Comment on the morphology of the red blood cells.
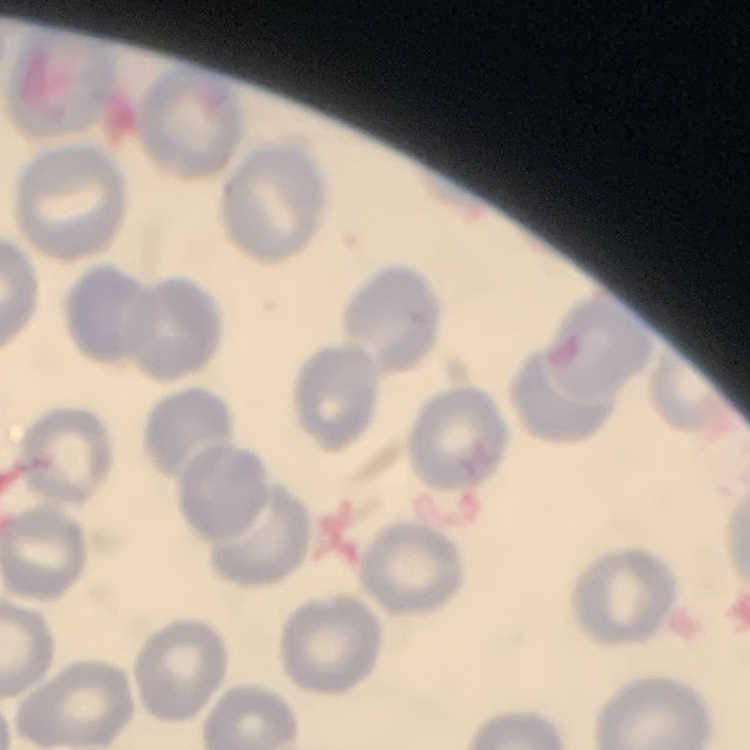
No rouleaux formation.

Summary:
  - Image type: one tile cut from a larger photomicrograph
  - Stain: Field's or Giemsa
  - Preparation: thin blood smear